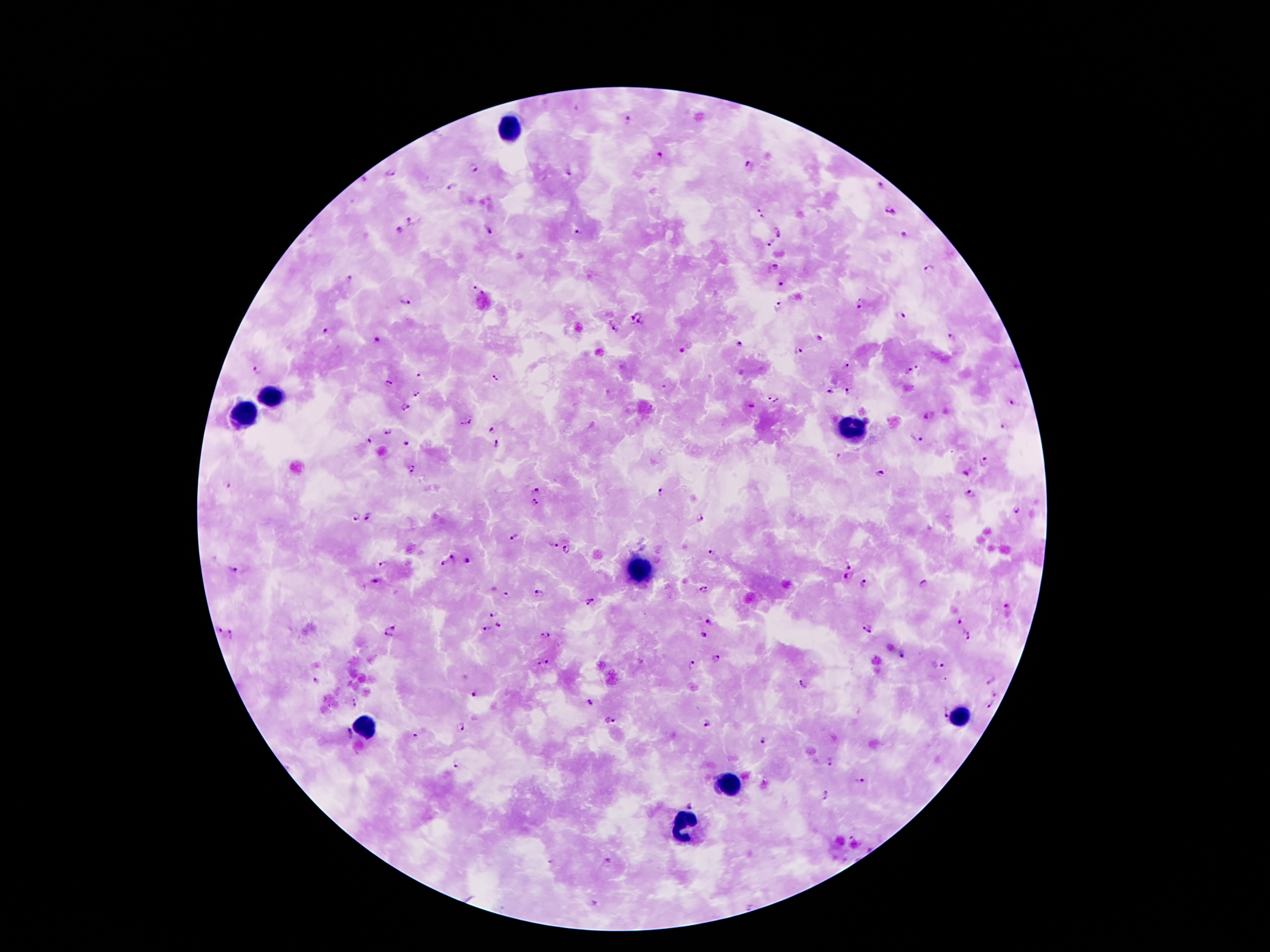
Approximate object centers, in pixels from the top-left corner.
Summary:
  - Leukocyte locations: (x=506, y=129), (x=271, y=395), (x=242, y=414), (x=849, y=431), (x=641, y=567), (x=958, y=719), (x=363, y=728), (x=727, y=786), (x=685, y=826)
  - Malaria parasite locations: (x=628, y=120), (x=659, y=155), (x=750, y=166), (x=473, y=168), (x=570, y=171), (x=390, y=175), (x=453, y=188), (x=878, y=188), (x=759, y=209), (x=891, y=210), (x=762, y=218), (x=411, y=220), (x=399, y=230), (x=489, y=231), (x=579, y=232), (x=779, y=232), (x=903, y=235), (x=771, y=241), (x=775, y=267), (x=930, y=268), (x=351, y=279), (x=781, y=284), (x=474, y=289), (x=405, y=303), (x=863, y=304), (x=777, y=306), (x=632, y=316), (x=899, y=316), (x=641, y=321), (x=615, y=328), (x=325, y=331), (x=954, y=336), (x=819, y=337), (x=378, y=341), (x=739, y=344), (x=680, y=351), (x=800, y=351), (x=847, y=365), (x=259, y=369), (x=918, y=369), (x=906, y=371), (x=419, y=375), (x=494, y=377), (x=389, y=384), (x=847, y=391), (x=832, y=392), (x=417, y=394), (x=770, y=398), (x=777, y=401), (x=1010, y=402), (x=404, y=407), (x=929, y=416), (x=471, y=421), (x=460, y=423), (x=1005, y=425), (x=493, y=430), (x=388, y=431), (x=370, y=439), (x=916, y=439), (x=406, y=442), (x=496, y=442), (x=984, y=463), (x=412, y=469), (x=879, y=474), (x=227, y=485), (x=536, y=490), (x=660, y=492), (x=971, y=494), (x=535, y=502), (x=1016, y=510), (x=356, y=516), (x=370, y=516), (x=703, y=518), (x=514, y=536), (x=553, y=545), (x=566, y=549), (x=713, y=552), (x=454, y=559), (x=468, y=560), (x=444, y=563), (x=382, y=564), (x=850, y=566), (x=234, y=570), (x=846, y=577), (x=375, y=580), (x=923, y=582), (x=865, y=583), (x=703, y=589), (x=505, y=593), (x=540, y=593), (x=591, y=603), (x=1008, y=606), (x=492, y=614), (x=961, y=621), (x=709, y=622), (x=498, y=625), (x=392, y=628), (x=866, y=628), (x=486, y=629), (x=220, y=630), (x=233, y=634), (x=388, y=635), (x=545, y=635), (x=703, y=635), (x=968, y=635), (x=903, y=654), (x=715, y=659), (x=547, y=662), (x=538, y=664), (x=938, y=665), (x=693, y=666), (x=992, y=680), (x=316, y=681), (x=803, y=684), (x=474, y=694), (x=995, y=694), (x=354, y=703), (x=591, y=705), (x=990, y=705), (x=943, y=712), (x=611, y=722), (x=706, y=724), (x=462, y=727), (x=348, y=732), (x=414, y=735), (x=761, y=741), (x=831, y=763), (x=456, y=766), (x=859, y=780), (x=827, y=796), (x=692, y=805), (x=851, y=838), (x=549, y=861), (x=608, y=862), (x=596, y=902)
  - Magnification: 100x
  - Patient malaria status: positive for Plasmodium falciparum
  - Field of view: single
  - Image size: 1270×952 pixels
  - Preparation: thick blood film
  - Stain: Giemsa
  - Capture: smartphone through the microscope eyepiece